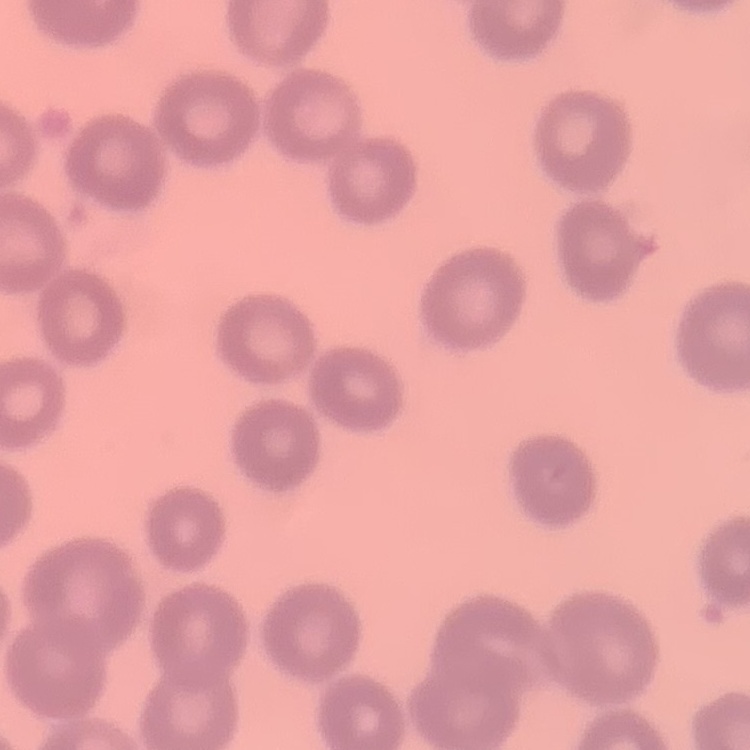
red blood cell morphology = no rouleaux formation
image type = square crop of a larger photomicrograph
stain = Field's or Giemsa
preparation = thin peripheral smear